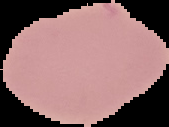
image type = segmented cell region on a black background
malaria status = uninfected
image size = 169×127 pixels
preparation = thin blood smear